Outline each blood parasite and name the species.
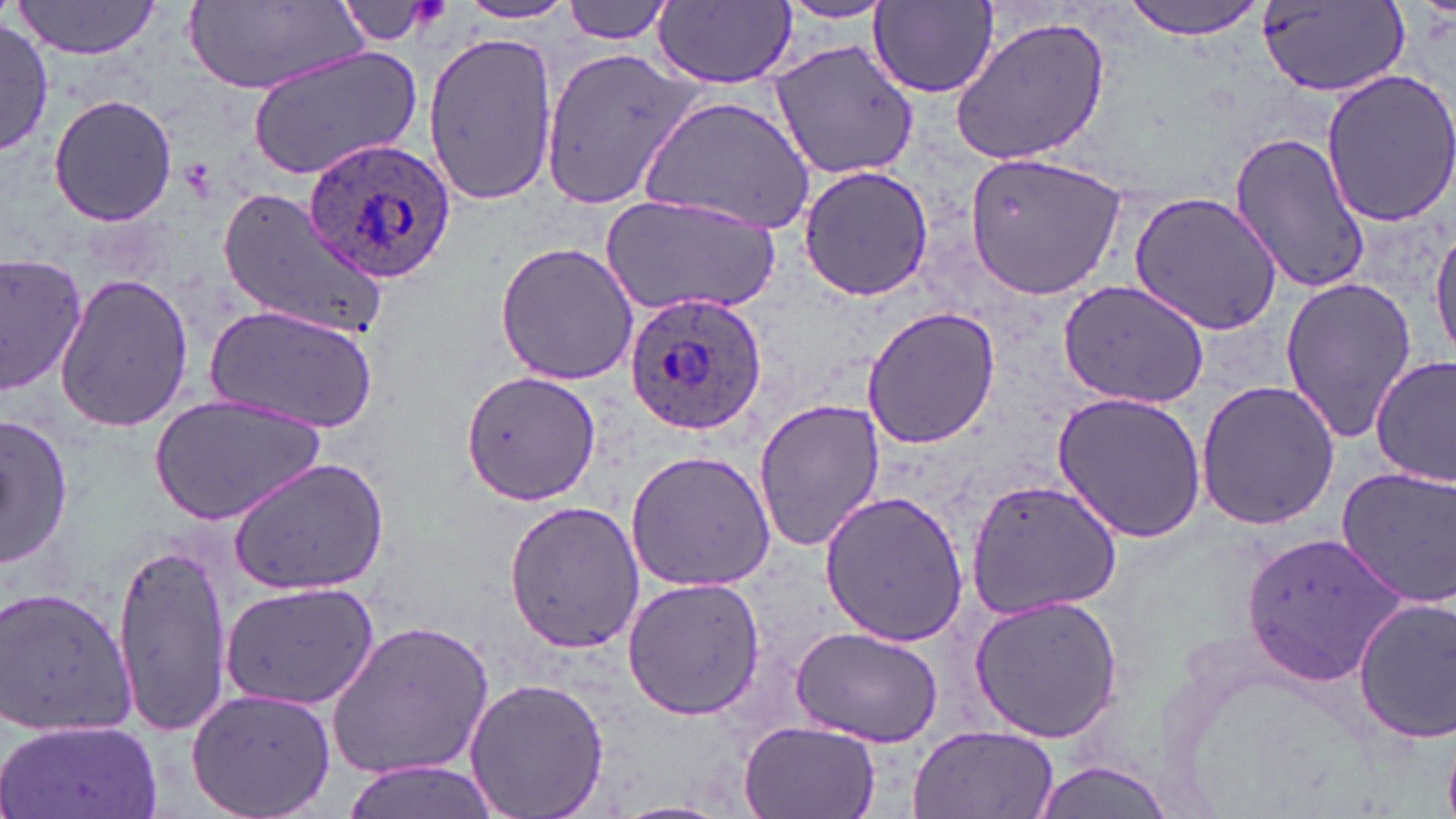

Approximate bounding boxes as (x1,y1)-(x2,y2) corner pairs in pixels.
Plasmodium ovale-infected red blood cells: (302,137)-(458,284), (624,292)-(769,436).
No Plasmodium falciparum, Plasmodium malariae, Plasmodium vivax, Babesia divergens, or Trypanosoma brucei observed.

{
  "slide_level_diagnosis": "Plasmodium ovale",
  "magnification": "1000x",
  "stain": "May-Grünwald-Giemsa",
  "field_of_view": "one of a larger specimen",
  "image_size": "1456×819 pixels",
  "modality": "light microscopy",
  "preparation": "thin blood smear",
  "uninfected_red_blood_cell_locations": "approximate bounding boxes as (x1,y1)-(x2,y2) corner pairs in pixels: (13,0)-(166,59), (561,0)-(679,44), (1122,0)-(1267,40), (182,1)-(363,92), (456,1)-(579,25), (653,1)-(795,87), (868,1)-(1001,98), (332,2)-(447,47), (772,2)-(897,24), (1261,2)-(1404,99), (949,16)-(1112,166), (0,18)-(51,158), (421,31)-(556,209), (768,40)-(921,180), (538,41)-(706,214), (247,47)-(423,181), (1321,67)-(1456,227), (48,94)-(179,227), (640,94)-(817,236), (1229,132)-(1371,295), (962,148)-(1130,302), (797,165)-(933,302), (220,190)-(388,340), (1131,190)-(1287,332), (600,192)-(783,316), (1431,219)-(1456,366), (494,240)-(639,386), (0,255)-(90,398), (54,273)-(193,431), (1279,277)-(1418,446), (1057,280)-(1212,409), (208,302)-(381,434), (861,307)-(1001,450), (1371,356)-(1454,487), (461,371)-(597,503), (1194,377)-(1342,531), (1052,390)-(1208,544), (150,396)-(326,525), (752,398)-(885,556), (1,413)-(73,571), (625,449)-(777,590), (227,459)-(389,595), (1336,466)-(1456,607), (964,479)-(1123,618), (817,490)-(969,647), (503,499)-(643,653), (1246,530)-(1411,686), (113,542)-(232,735), (621,577)-(767,722), (220,582)-(381,709), (1,585)-(137,736), (969,594)-(1124,744), (1352,596)-(1456,747), (326,617)-(495,783), (792,627)-(944,749), (465,676)-(608,819), (184,685)-(337,819), (1,718)-(165,819), (735,720)-(882,819), (908,726)-(1060,817), (335,759)-(507,819), (1028,759)-(1177,819)"
}